Describe the morphology of the erythrocytes.
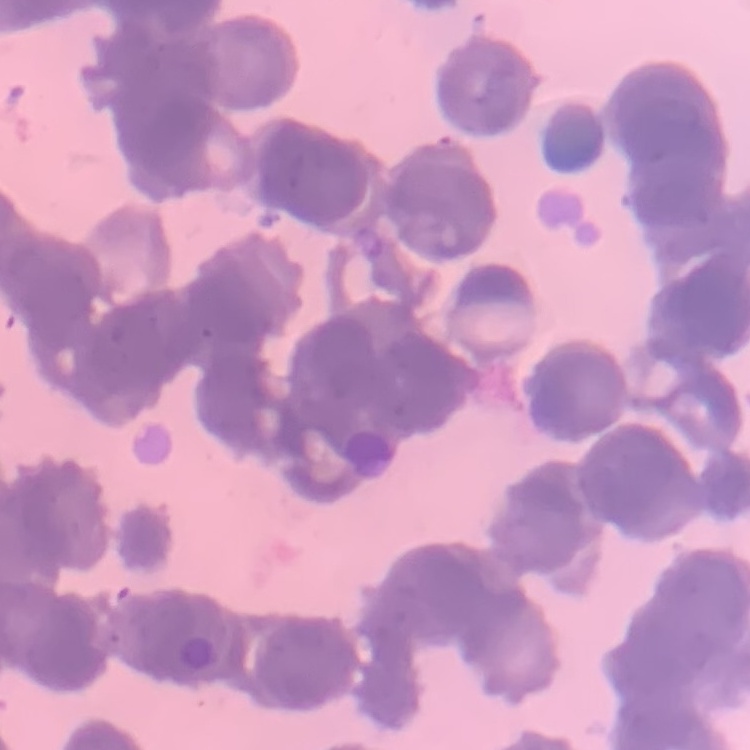

Rouleaux formation.

{
  "stain": "Field's or Giemsa",
  "image_type": "one tile cut from a larger photomicrograph",
  "preparation": "thin blood smear"
}